Identify the blood parasite species.
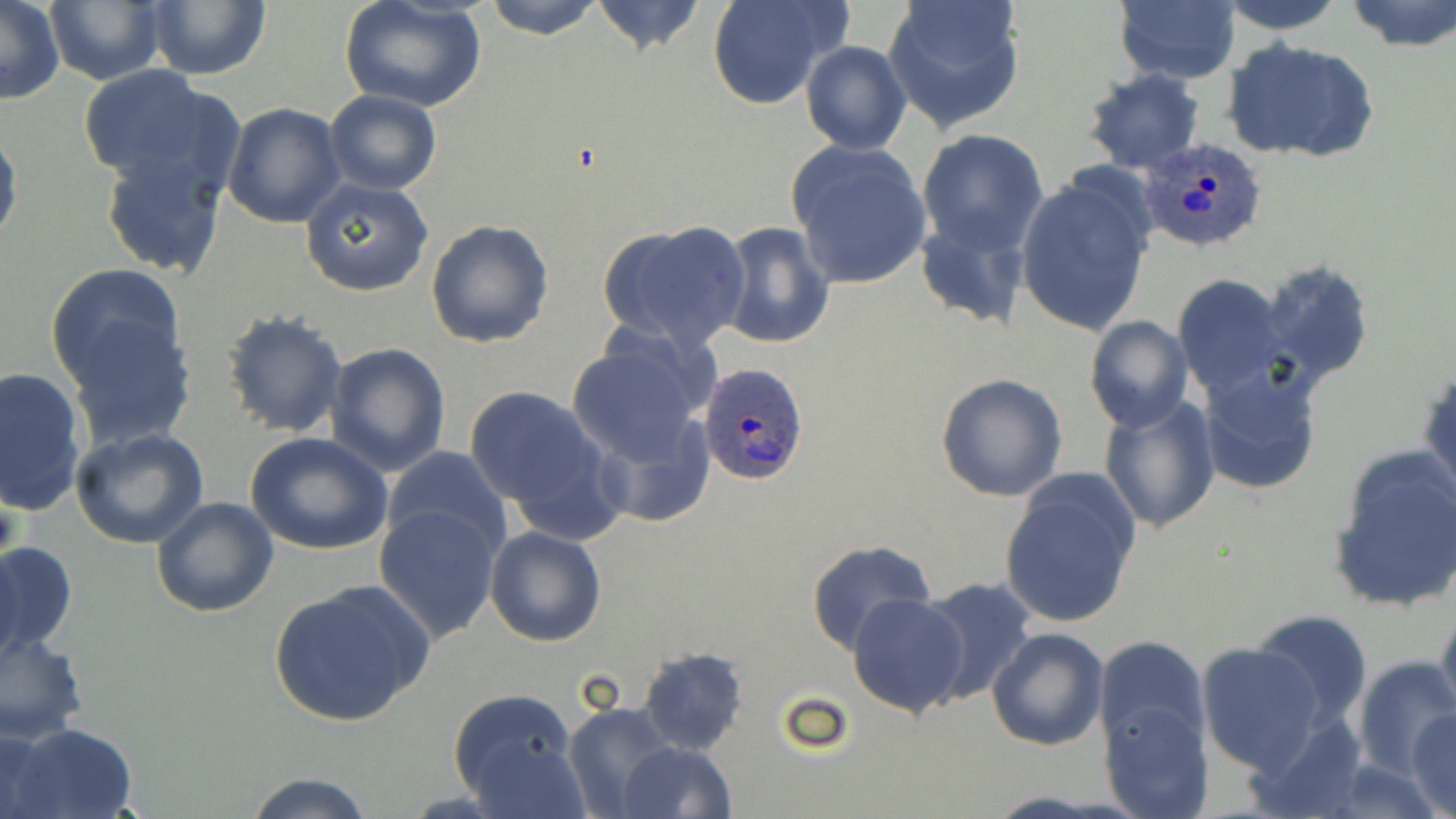
Plasmodium ovale.

Approximate bounding boxes as (x1,y1)-(x2,y2) corner pairs in pixels. Plasmodium ovale-infected red blood cell locations: (1138,137)-(1271,252), (699,361)-(808,486). Uninfected red blood cell locations: (0,0)-(64,105), (44,0)-(166,86), (141,0)-(271,81), (337,0)-(489,113), (483,0)-(605,38), (589,0)-(708,56), (707,0)-(847,110), (881,0)-(1027,134), (1219,0)-(1347,35), (1345,0)-(1456,51), (1114,1)-(1241,85), (801,39)-(911,155), (1223,39)-(1379,163), (75,65)-(240,197), (1081,69)-(1205,175), (324,89)-(442,194), (223,102)-(347,228), (0,121)-(22,255), (918,126)-(1048,255), (787,142)-(933,289), (98,146)-(230,279), (1015,174)-(1155,336), (301,178)-(435,296), (914,216)-(1033,332), (425,219)-(553,348), (596,220)-(752,352), (717,221)-(834,351), (1259,260)-(1375,389), (45,263)-(187,394), (1172,274)-(1290,399), (218,307)-(349,437), (1084,316)-(1193,433), (62,317)-(198,450), (565,336)-(714,468), (324,343)-(451,476), (1420,359)-(1455,508), (1197,362)-(1323,496), (0,366)-(89,518), (937,372)-(1068,503), (464,386)-(609,514), (1097,394)-(1221,535), (586,412)-(713,529), (71,427)-(209,549), (245,432)-(393,555), (382,445)-(511,557), (1326,446)-(1456,613), (998,473)-(1140,631), (150,496)-(279,618), (375,505)-(502,641), (484,526)-(607,647), (0,539)-(79,663), (805,539)-(936,653), (912,577)-(1039,704), (270,580)-(431,729), (847,593)-(969,718), (1436,603)-(1456,726), (1250,608)-(1374,731), (989,627)-(1109,749), (1,630)-(88,744), (1094,636)-(1209,756), (1196,641)-(1327,774), (637,647)-(749,754), (1352,655)-(1455,779), (447,689)-(582,807), (563,700)-(681,817), (1103,701)-(1212,818), (1409,708)-(1456,818), (9,723)-(138,818), (1,726)-(55,817), (617,739)-(736,819), (240,773)-(381,819). Thin blood film. One field of a larger specimen. Image is 1456×819 pixels. Light microscopy. 1000x magnification. May-Grünwald-Giemsa stain.